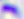
Captured at 400x magnification. Toxoplasma gondii is shown. Micrograph.